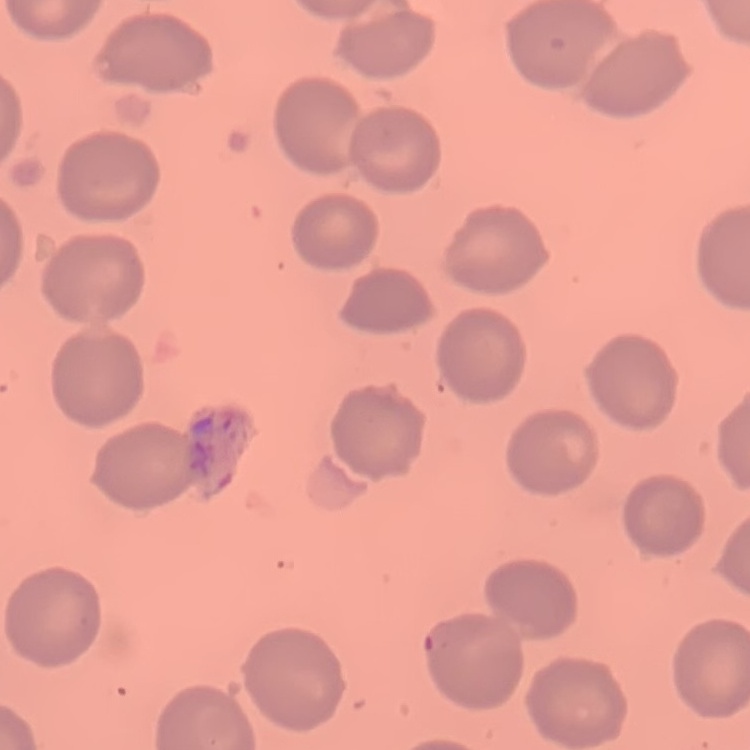

Summary:
  - Erythrocyte morphology: no rouleaux formation
  - Image type: square crop of a larger photomicrograph
  - Preparation: thin peripheral smear
  - Stain: Field's or Giemsa